Assess this cell for malaria.
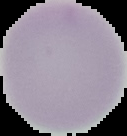
It is uninfected.

Image is 127×136 pixels. Segmented cell region on a black background. From a thin blood film.